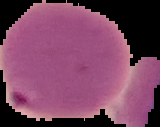 Image is 160×127 pixels. From a thin blood smear. Malaria status: parasitized. Cell region segmented out of the field of view; the surrounding area is masked to black.